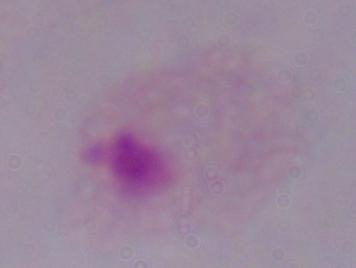
Summary:
  - Modality: micrograph
  - Magnification: 1000x
  - Identification: trichomonad